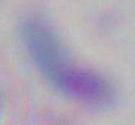
1000x magnification. Photomicrograph. Toxoplasma gondii is seen.